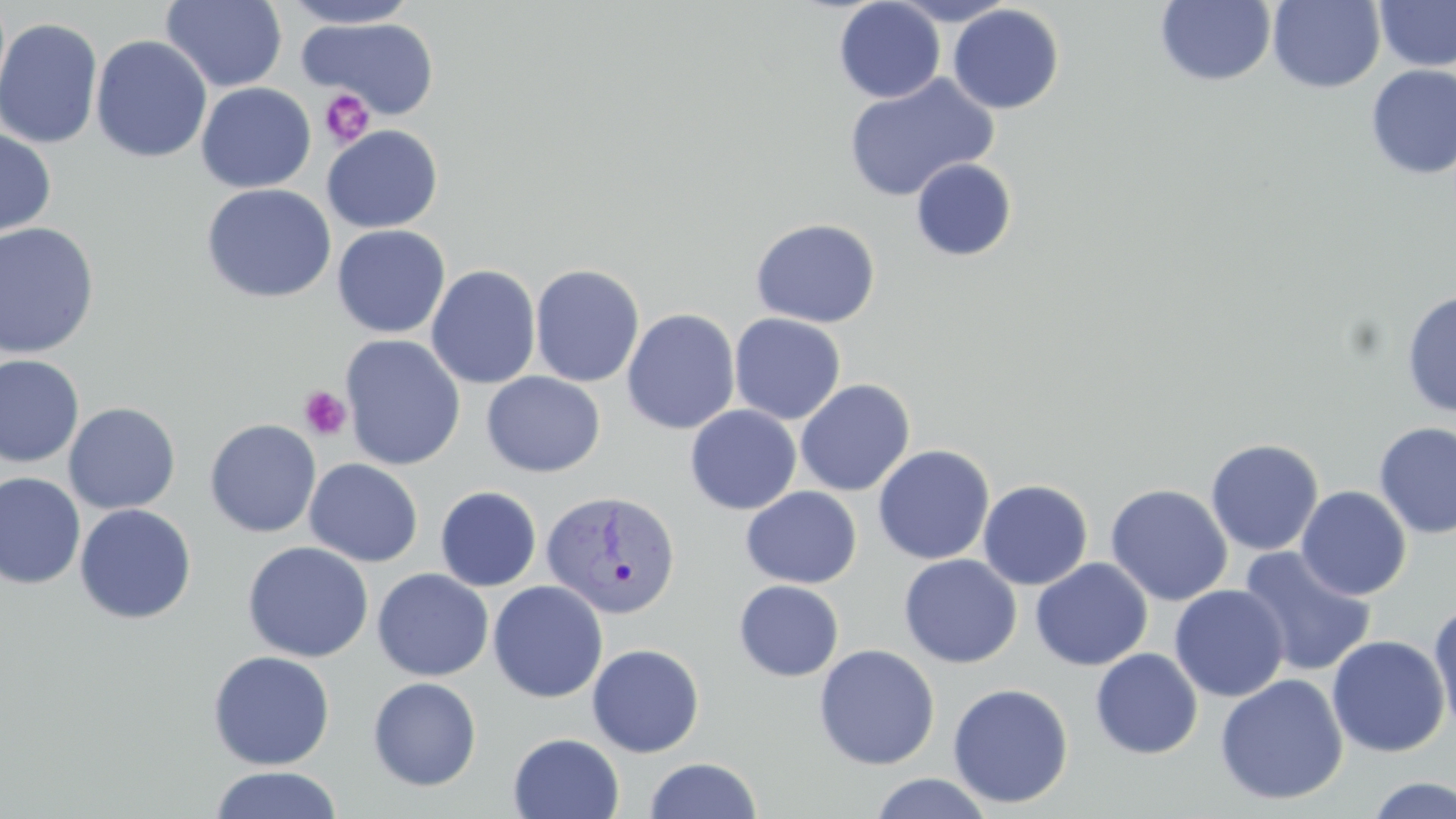
slide-level diagnosis = Plasmodium vivax
image size = 1456×819 pixels
preparation = thin blood film
platelet locations = approximate bounding boxes as named x1/y1/x2/y2 corners in pixels: (x1=319, y1=89, x2=375, y2=149), (x1=298, y1=385, x2=352, y2=441)
magnification = 1000x
stain = May-Grünwald-Giemsa
uninfected red blood cell locations = approximate bounding boxes as named x1/y1/x2/y2 corners in pixels: (x1=161, y1=0, x2=288, y2=92), (x1=279, y1=0, x2=422, y2=28), (x1=886, y1=0, x2=1020, y2=25), (x1=1374, y1=0, x2=1456, y2=71), (x1=833, y1=1, x2=945, y2=103), (x1=1154, y1=1, x2=1277, y2=87), (x1=1267, y1=1, x2=1385, y2=93), (x1=947, y1=4, x2=1065, y2=114), (x1=299, y1=16, x2=440, y2=120), (x1=0, y1=17, x2=103, y2=150), (x1=91, y1=35, x2=212, y2=163), (x1=1365, y1=65, x2=1456, y2=178), (x1=842, y1=73, x2=998, y2=202), (x1=196, y1=82, x2=316, y2=193), (x1=321, y1=125, x2=443, y2=233), (x1=0, y1=127, x2=57, y2=240), (x1=910, y1=158, x2=1018, y2=261), (x1=200, y1=183, x2=337, y2=304), (x1=750, y1=218, x2=881, y2=328), (x1=0, y1=222, x2=101, y2=359), (x1=332, y1=224, x2=450, y2=339), (x1=530, y1=263, x2=645, y2=388), (x1=426, y1=264, x2=541, y2=389), (x1=1401, y1=289, x2=1456, y2=418), (x1=622, y1=308, x2=740, y2=435), (x1=729, y1=313, x2=846, y2=425), (x1=339, y1=334, x2=466, y2=471), (x1=0, y1=354, x2=85, y2=468), (x1=481, y1=371, x2=605, y2=478), (x1=794, y1=379, x2=915, y2=497), (x1=63, y1=402, x2=181, y2=515), (x1=685, y1=405, x2=802, y2=515), (x1=204, y1=419, x2=321, y2=538), (x1=1374, y1=422, x2=1456, y2=540), (x1=1205, y1=438, x2=1324, y2=555), (x1=873, y1=444, x2=994, y2=565), (x1=304, y1=458, x2=424, y2=567), (x1=0, y1=473, x2=86, y2=589), (x1=977, y1=479, x2=1093, y2=590), (x1=1105, y1=483, x2=1233, y2=606), (x1=434, y1=486, x2=542, y2=592), (x1=741, y1=486, x2=862, y2=588), (x1=1296, y1=486, x2=1411, y2=600), (x1=74, y1=503, x2=197, y2=625), (x1=242, y1=541, x2=374, y2=663), (x1=1238, y1=545, x2=1376, y2=678), (x1=899, y1=554, x2=1022, y2=668), (x1=1030, y1=558, x2=1153, y2=671), (x1=372, y1=569, x2=494, y2=681), (x1=487, y1=580, x2=609, y2=703), (x1=733, y1=580, x2=844, y2=681), (x1=1169, y1=584, x2=1290, y2=702), (x1=1429, y1=601, x2=1456, y2=738), (x1=1327, y1=634, x2=1450, y2=758), (x1=587, y1=643, x2=705, y2=757), (x1=814, y1=644, x2=940, y2=770), (x1=1090, y1=648, x2=1203, y2=759), (x1=208, y1=650, x2=335, y2=771), (x1=1215, y1=674, x2=1349, y2=805), (x1=367, y1=677, x2=482, y2=792), (x1=947, y1=682, x2=1074, y2=809), (x1=508, y1=732, x2=625, y2=819), (x1=644, y1=757, x2=762, y2=818), (x1=209, y1=766, x2=343, y2=819), (x1=868, y1=773, x2=995, y2=818), (x1=1364, y1=776, x2=1456, y2=818)
modality = optical microscopy
field of view = single
Plasmodium vivax-infected red blood cell locations = approximate bounding boxes as named x1/y1/x2/y2 corners in pixels: (x1=541, y1=491, x2=681, y2=620)